Locate the red blood cells and classify each one as P. falciparum-infected, uninfected, or of indeterminate infection status.
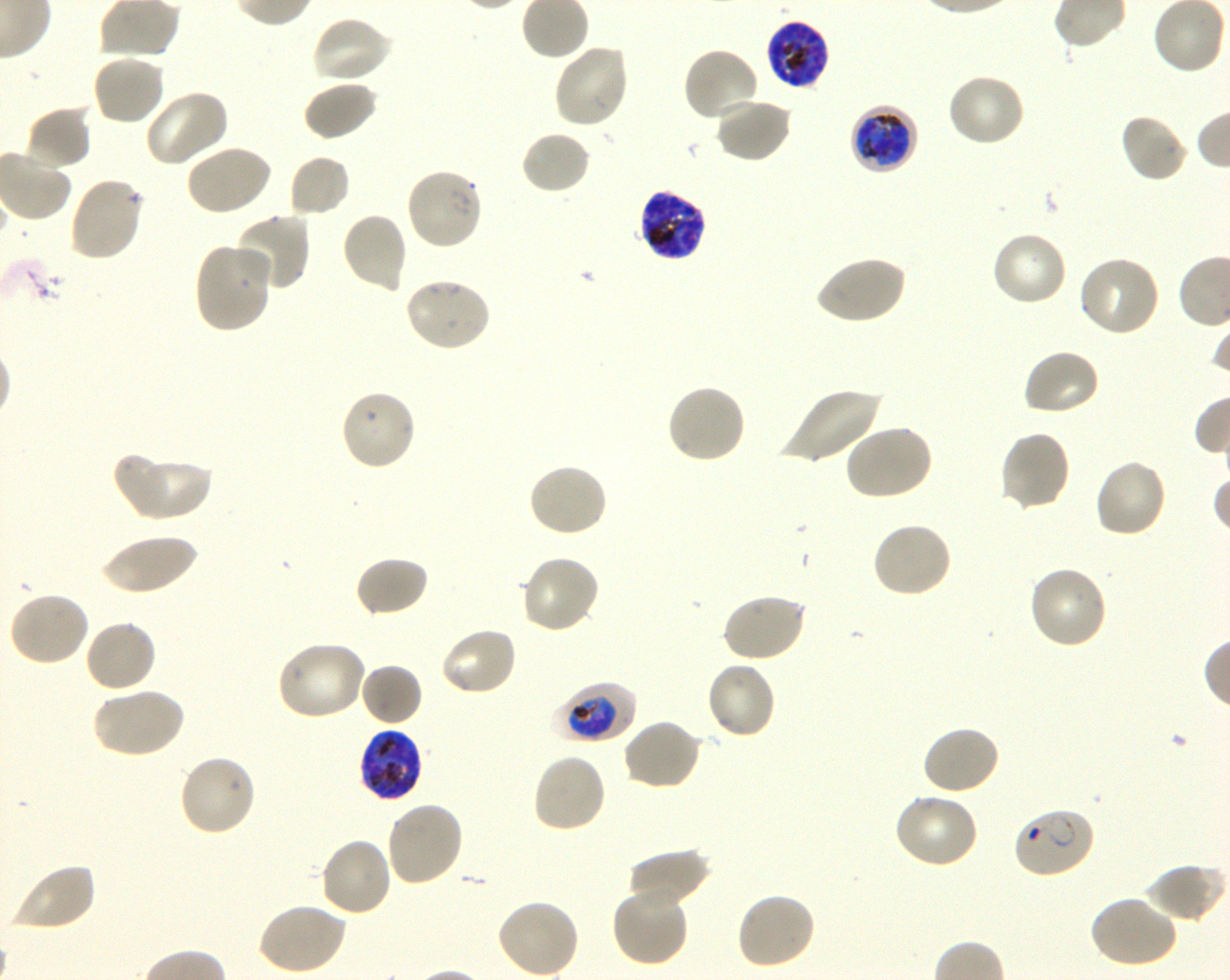
Approximate bounding boxes as {x1, y1, x2, y2} in pixels. Not every red blood cell is marked. A life-cycle stage — or a range of stages, where the recorded stages span more than one — follows each staged infected red blood cell.
Infected red blood cells: {764, 17, 831, 91} late trophozoite to late schizont; {850, 105, 919, 175} late trophozoite to late schizont; {638, 188, 708, 262} late trophozoite to late schizont; {552, 680, 637, 744} trophozoite; {358, 728, 423, 803} late trophozoite to late schizont; {1012, 807, 1098, 880} ring.
Uninfected red blood cells: {311, 15, 394, 86}, {552, 43, 630, 129}, {682, 46, 762, 122}, {91, 53, 166, 127}, {946, 73, 1026, 148}, {302, 79, 379, 141}, {144, 89, 231, 168}, {713, 97, 793, 164}, {24, 106, 93, 173}, {1119, 112, 1190, 184}, {520, 129, 591, 195}, {185, 143, 273, 217}, {288, 154, 351, 218}, {404, 167, 484, 252}, {68, 176, 145, 263}, {340, 211, 409, 293}, {232, 213, 311, 293}, {990, 231, 1068, 308}, {193, 242, 274, 333}, {814, 254, 907, 326}, {1077, 255, 1162, 338}, {403, 277, 493, 354}, {1021, 348, 1102, 418}, {665, 383, 747, 465}, {780, 386, 883, 467}, {339, 388, 417, 472}, {842, 424, 933, 501}, {998, 430, 1071, 512}, {118, 454, 212, 521}, {1093, 457, 1169, 539}, {526, 463, 609, 538}, {871, 522, 953, 600}, {101, 534, 200, 596}, {520, 553, 601, 634}, {354, 555, 430, 619}, {1028, 565, 1109, 651}, {8, 591, 91, 668}, {720, 592, 808, 663}, {83, 618, 158, 693}, {439, 625, 518, 697}, {275, 639, 368, 721}, {705, 660, 777, 741}, {359, 663, 423, 727}, {90, 685, 185, 760}, {622, 718, 703, 791}, {921, 724, 1002, 796}, {531, 752, 608, 834}, {177, 753, 258, 837}, {892, 791, 979, 869}, {385, 800, 465, 888}, {318, 836, 394, 918}, {627, 848, 710, 908}, {10, 862, 97, 932}, {1143, 863, 1224, 923}, {610, 884, 690, 967}, {735, 891, 816, 971}, {1087, 895, 1178, 969}, {496, 897, 580, 978}, {257, 902, 348, 975}.
No red blood cells of indeterminate infection status observed.

Summary:
  - Image size: 1230×980 pixels
  - Life-cycle stages observed: ring, trophozoite
  - Donor blood group: O+
  - Stain: Giemsa
  - Preparation: thin blood smear
  - Culture: P. falciparum strain 3D7, shaking, in vitro
  - Field of view: one from this slide
  - Objective: 100x, oil immersion, numerical aperture 1.30